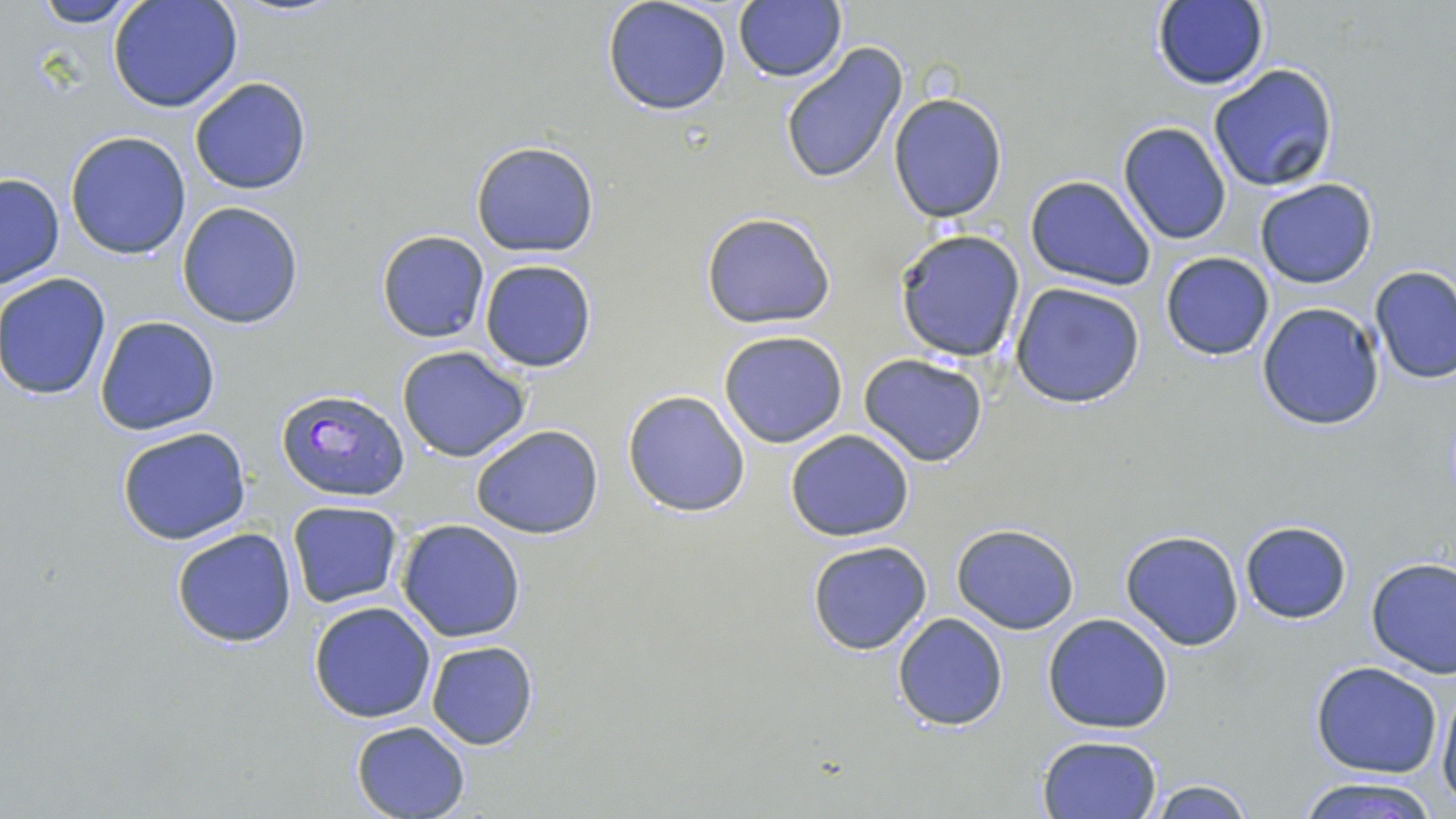

slide-level diagnosis = Plasmodium falciparum
modality = optical microscopy
uninfected red blood cell locations = approximate bounding boxes as (x1, y1, x2, y2) in pixels: (24, 0, 144, 26), (107, 0, 244, 114), (602, 0, 733, 116), (1150, 1, 1269, 90), (734, 3, 847, 82), (779, 40, 910, 184), (1208, 63, 1339, 192), (189, 77, 312, 194), (888, 93, 1008, 223), (1119, 122, 1231, 245), (66, 130, 191, 259), (470, 140, 599, 258), (0, 174, 65, 290), (1025, 175, 1155, 290), (1254, 177, 1378, 289), (177, 201, 304, 329), (699, 211, 838, 330), (893, 228, 1026, 361), (376, 229, 489, 343), (1159, 252, 1274, 360), (479, 260, 598, 372), (1369, 265, 1456, 384), (1, 273, 112, 399), (1010, 283, 1148, 408), (1256, 302, 1386, 431), (96, 315, 221, 435), (719, 329, 848, 449), (396, 346, 532, 463), (858, 353, 989, 466), (621, 388, 752, 517), (116, 424, 252, 546), (470, 424, 604, 539), (785, 429, 915, 542), (286, 501, 403, 607), (396, 519, 525, 643), (1239, 521, 1352, 624), (951, 523, 1079, 634), (170, 527, 297, 648), (1119, 530, 1245, 650), (806, 539, 935, 656), (1366, 556, 1456, 677), (308, 600, 437, 722), (893, 611, 1008, 730), (1042, 613, 1174, 734), (425, 640, 538, 749), (1310, 661, 1443, 778), (1437, 681, 1456, 810), (349, 719, 473, 818), (1037, 734, 1164, 819), (1294, 777, 1441, 819), (1141, 778, 1258, 818)
preparation = thin blood film
magnification = 1000x
field of view = one of a larger specimen
Plasmodium falciparum-infected red blood cell locations = approximate bounding boxes as (x1, y1, x2, y2) in pixels: (276, 385, 409, 500)
image size = 1456×819 pixels
stain = May-Grünwald-Giemsa